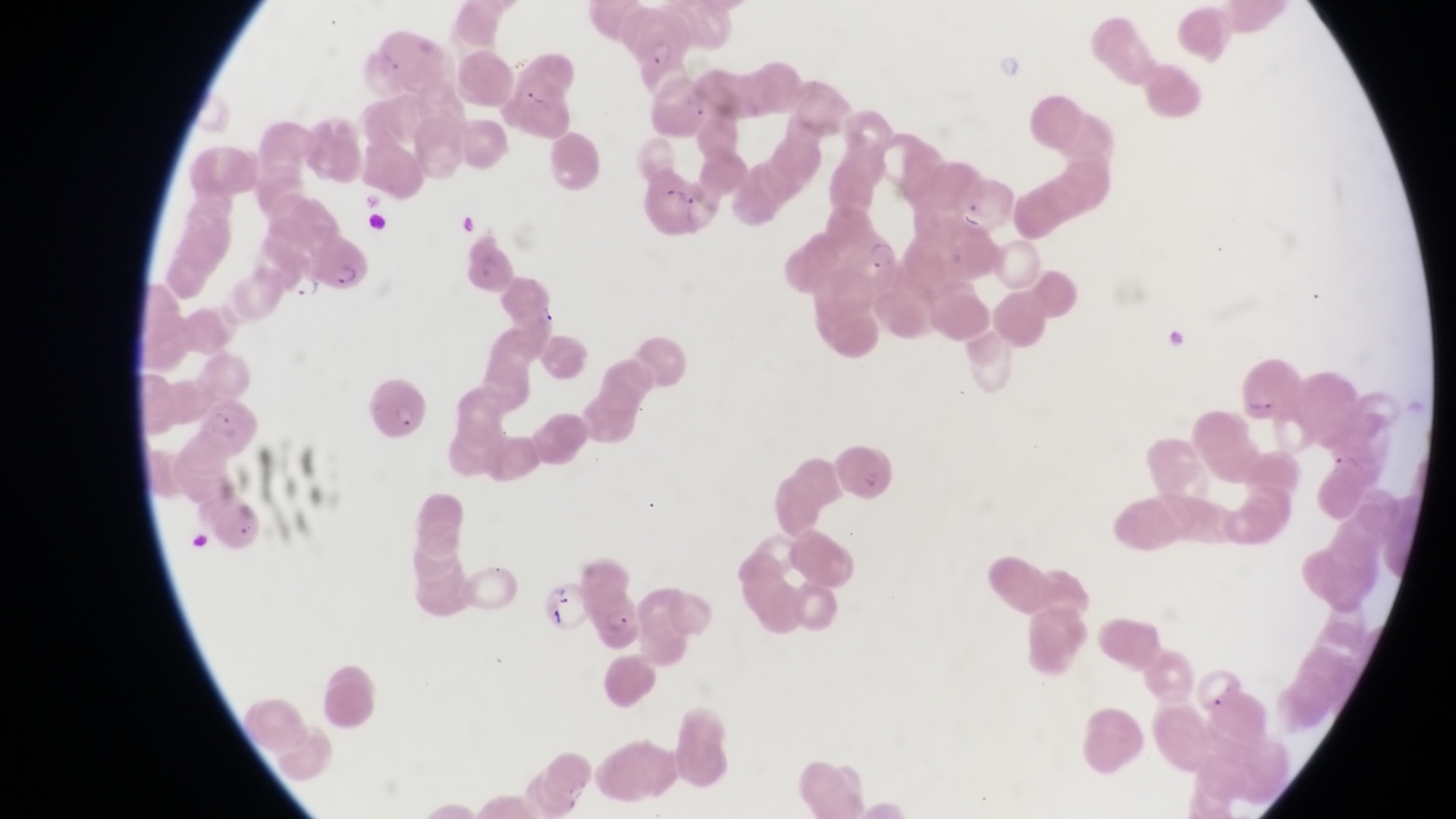
trophozoite locations = approximate bounding boxes as [left, top, right, bottom] in pixels: [868, 238, 901, 271], [290, 272, 323, 304]
preparation = thin blood film
country = Uganda
capture = smartphone photograph through the eyepiece of an Olympus CX-23 microscope
field of view = single
artifact (platelet-like body, stain precipitate, or debris) locations = approximate bounding boxes as [left, top, right, bottom] in pixels: [457, 208, 483, 241]
magnification = 1000x
image size = 1456×819 pixels
parasitised red blood cell locations = approximate bounding boxes as [left, top, right, bottom] in pixels: [614, 8, 693, 85], [642, 171, 700, 234], [309, 228, 368, 292], [497, 271, 560, 331], [369, 381, 430, 441], [541, 578, 588, 634], [597, 587, 646, 658]